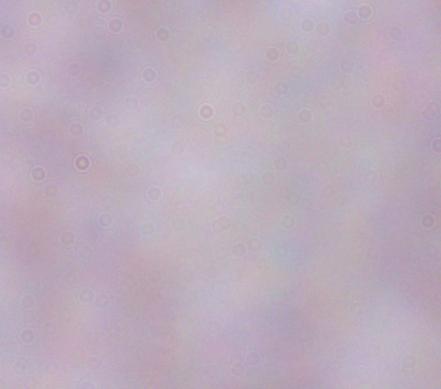
Summary:
  - Magnification: 1000x
  - Modality: photomicrograph
  - Identification: trypanosome